Locate every Plasmodium falciparum-infected red blood cell.
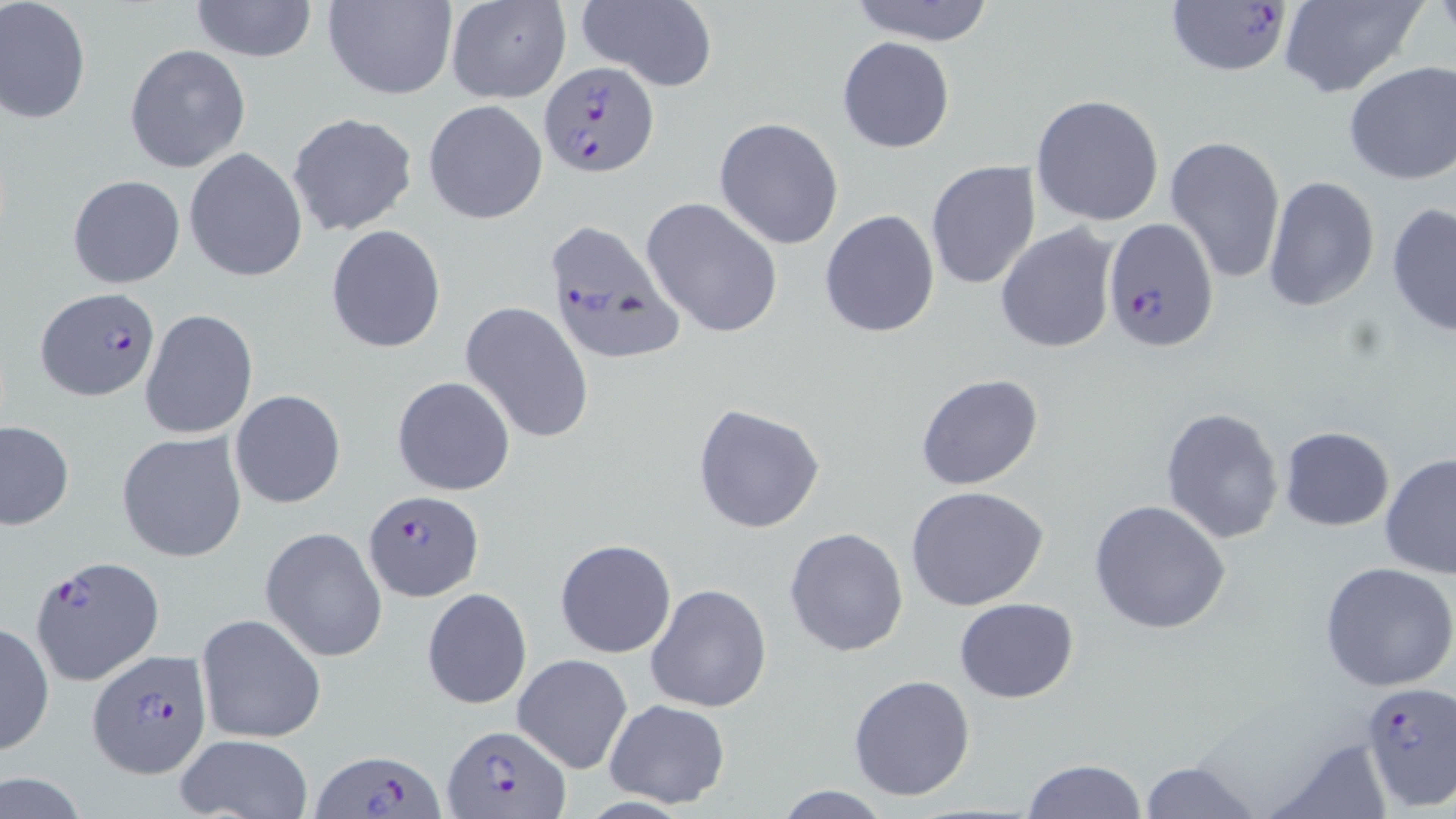
Approximate bounding boxes as (x1, y1, x2, y2) in pixels.
Plasmodium falciparum-infected red blood cells: (1166, 0, 1292, 78), (537, 60, 658, 177), (1102, 216, 1219, 353), (540, 217, 686, 368), (35, 289, 159, 401), (362, 489, 484, 601), (31, 555, 163, 685), (86, 647, 212, 778), (1358, 684, 1455, 809), (440, 724, 567, 816), (315, 748, 444, 819).

Uninfected red blood cell locations: (0, 0, 91, 124), (188, 0, 317, 63), (322, 0, 458, 101), (446, 0, 569, 103), (572, 0, 718, 91), (841, 0, 1001, 46), (1278, 0, 1429, 100), (836, 36, 956, 154), (124, 43, 252, 174), (1342, 60, 1456, 186), (1031, 94, 1165, 227), (423, 99, 548, 224), (286, 112, 420, 238), (713, 117, 844, 250), (1163, 135, 1286, 284), (184, 148, 307, 283), (925, 159, 1042, 291), (68, 175, 185, 288), (1262, 176, 1380, 311), (641, 196, 784, 338), (1386, 200, 1456, 339), (819, 209, 941, 339), (994, 222, 1120, 357), (326, 225, 447, 354), (460, 301, 594, 444), (140, 308, 258, 439), (915, 373, 1045, 491), (392, 376, 516, 496), (230, 389, 347, 509), (691, 404, 825, 534), (1161, 405, 1287, 545), (0, 420, 74, 530), (1279, 426, 1393, 531), (117, 431, 247, 563), (1380, 451, 1456, 579), (906, 486, 1051, 612), (1089, 498, 1231, 635), (261, 526, 388, 662), (784, 527, 910, 658), (554, 537, 677, 659), (1319, 561, 1456, 692), (647, 583, 772, 713), (422, 587, 532, 709), (954, 597, 1079, 703), (195, 613, 326, 745), (0, 622, 54, 757), (512, 654, 633, 772), (847, 673, 976, 801), (602, 700, 731, 807), (174, 734, 312, 819), (1265, 739, 1391, 816), (1022, 758, 1149, 818), (1138, 759, 1262, 818), (1, 773, 92, 818), (771, 786, 897, 818). Slide-level diagnosis: Plasmodium falciparum. Image is 1456×819 pixels. Optical microscopy. May-Grünwald-Giemsa stain. Captured at 1000x magnification. Thin blood film. Single field of view.